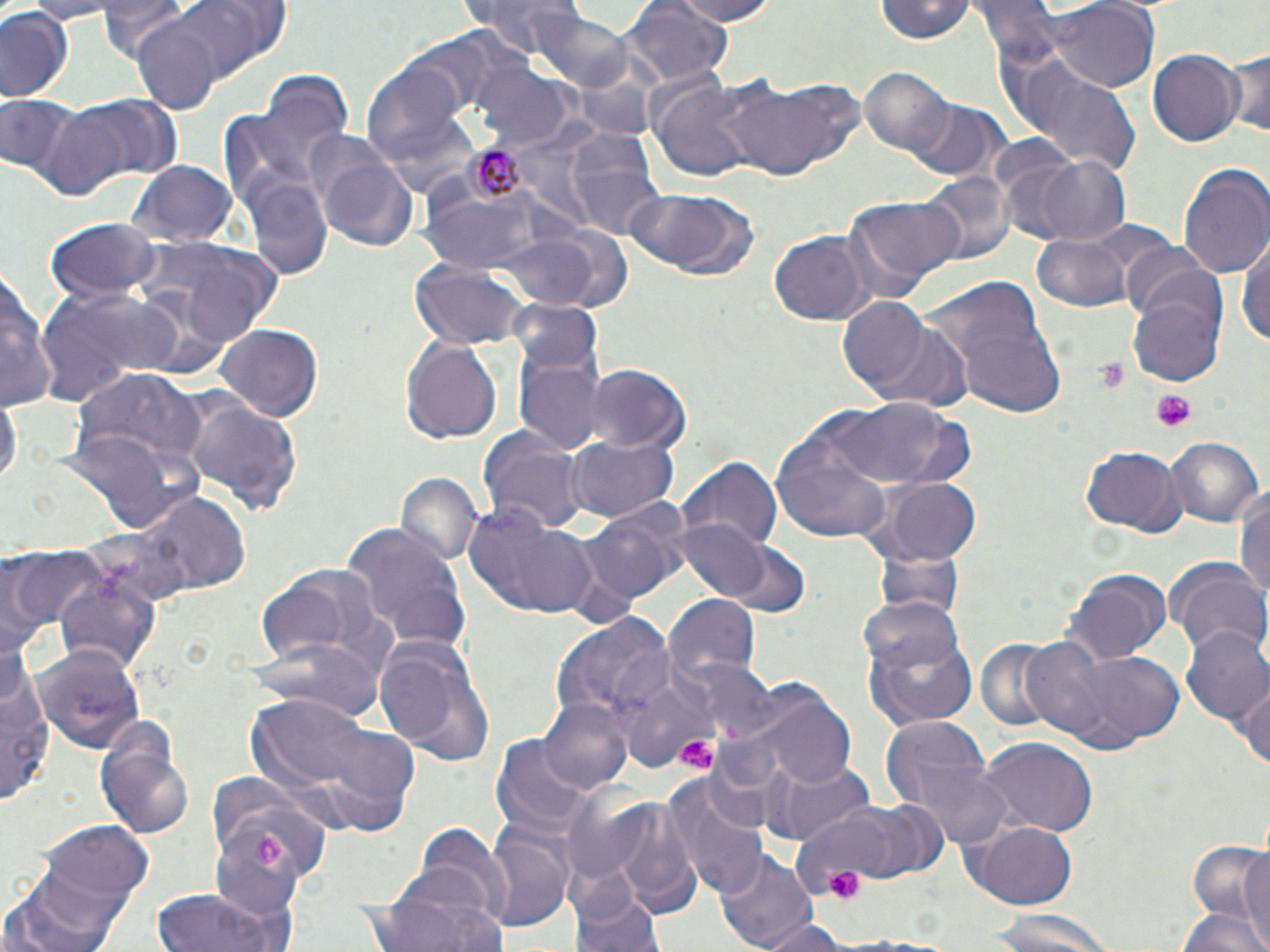 Approximate bounding boxes as named x1/y1/x2/y2 corners in pixels. Plasmodium malariae-infected red blood cell locations: (x1=459, y1=137, x2=545, y2=210). Uninfected red blood cell locations: (x1=93, y1=0, x2=203, y2=71), (x1=159, y1=0, x2=290, y2=78), (x1=453, y1=0, x2=593, y2=49), (x1=662, y1=0, x2=787, y2=25), (x1=872, y1=0, x2=978, y2=45), (x1=625, y1=1, x2=732, y2=87), (x1=0, y1=4, x2=75, y2=106), (x1=1047, y1=4, x2=1159, y2=92), (x1=536, y1=8, x2=634, y2=92), (x1=131, y1=20, x2=219, y2=112), (x1=1224, y1=47, x2=1269, y2=141), (x1=1147, y1=51, x2=1242, y2=146), (x1=1002, y1=54, x2=1141, y2=174), (x1=473, y1=63, x2=569, y2=147), (x1=361, y1=64, x2=459, y2=154), (x1=246, y1=65, x2=354, y2=184), (x1=859, y1=69, x2=956, y2=159), (x1=713, y1=77, x2=856, y2=184), (x1=653, y1=79, x2=761, y2=182), (x1=49, y1=94, x2=181, y2=192), (x1=1, y1=95, x2=79, y2=182), (x1=909, y1=101, x2=1005, y2=182), (x1=564, y1=128, x2=665, y2=236), (x1=306, y1=132, x2=420, y2=253), (x1=1028, y1=155, x2=1133, y2=246), (x1=1178, y1=159, x2=1270, y2=279), (x1=128, y1=162, x2=236, y2=249), (x1=922, y1=170, x2=1010, y2=268), (x1=246, y1=179, x2=334, y2=280), (x1=622, y1=188, x2=761, y2=282), (x1=404, y1=191, x2=540, y2=261), (x1=849, y1=195, x2=967, y2=290), (x1=46, y1=219, x2=161, y2=302), (x1=557, y1=221, x2=641, y2=314), (x1=770, y1=232, x2=871, y2=326), (x1=1033, y1=234, x2=1133, y2=312), (x1=1236, y1=234, x2=1270, y2=352), (x1=130, y1=237, x2=286, y2=351), (x1=1121, y1=241, x2=1215, y2=323), (x1=409, y1=259, x2=529, y2=347), (x1=0, y1=266, x2=53, y2=415), (x1=922, y1=271, x2=1072, y2=423), (x1=1125, y1=273, x2=1230, y2=388), (x1=34, y1=283, x2=189, y2=402), (x1=835, y1=294, x2=946, y2=405), (x1=510, y1=320, x2=609, y2=457), (x1=215, y1=326, x2=323, y2=420), (x1=400, y1=337, x2=503, y2=446), (x1=583, y1=362, x2=691, y2=454), (x1=70, y1=370, x2=208, y2=481), (x1=176, y1=392, x2=305, y2=522), (x1=0, y1=394, x2=20, y2=493), (x1=827, y1=397, x2=970, y2=491), (x1=771, y1=426, x2=895, y2=543), (x1=481, y1=428, x2=585, y2=534), (x1=56, y1=430, x2=183, y2=536), (x1=566, y1=436, x2=678, y2=523), (x1=1166, y1=437, x2=1263, y2=530), (x1=1082, y1=447, x2=1185, y2=535), (x1=678, y1=455, x2=780, y2=553), (x1=395, y1=473, x2=483, y2=571), (x1=866, y1=478, x2=983, y2=561), (x1=1236, y1=484, x2=1270, y2=612), (x1=120, y1=487, x2=250, y2=602), (x1=466, y1=501, x2=597, y2=621), (x1=577, y1=506, x2=683, y2=605), (x1=677, y1=519, x2=770, y2=600), (x1=342, y1=522, x2=472, y2=653), (x1=871, y1=535, x2=963, y2=618), (x1=724, y1=544, x2=811, y2=620), (x1=7, y1=546, x2=110, y2=637), (x1=1168, y1=560, x2=1270, y2=662), (x1=257, y1=565, x2=388, y2=671), (x1=1064, y1=569, x2=1171, y2=666), (x1=55, y1=571, x2=161, y2=676), (x1=663, y1=595, x2=759, y2=687), (x1=552, y1=614, x2=675, y2=734), (x1=862, y1=616, x2=982, y2=730), (x1=1182, y1=626, x2=1270, y2=726), (x1=372, y1=631, x2=495, y2=765), (x1=973, y1=638, x2=1067, y2=732), (x1=35, y1=643, x2=145, y2=754), (x1=1049, y1=643, x2=1189, y2=753), (x1=610, y1=655, x2=720, y2=772), (x1=2, y1=666, x2=54, y2=811), (x1=1232, y1=676, x2=1270, y2=771), (x1=753, y1=689, x2=858, y2=788), (x1=245, y1=693, x2=418, y2=838), (x1=540, y1=697, x2=632, y2=795), (x1=882, y1=716, x2=988, y2=813), (x1=94, y1=725, x2=195, y2=837), (x1=491, y1=734, x2=594, y2=837), (x1=981, y1=737, x2=1096, y2=837), (x1=910, y1=756, x2=1019, y2=849), (x1=765, y1=758, x2=873, y2=844), (x1=664, y1=770, x2=768, y2=895), (x1=598, y1=800, x2=704, y2=916), (x1=844, y1=800, x2=951, y2=883), (x1=962, y1=820, x2=1080, y2=910), (x1=37, y1=822, x2=151, y2=909), (x1=206, y1=823, x2=304, y2=917), (x1=409, y1=823, x2=512, y2=922), (x1=480, y1=829, x2=573, y2=932), (x1=1233, y1=850, x2=1270, y2=946), (x1=713, y1=851, x2=818, y2=952), (x1=1181, y1=863, x2=1268, y2=948), (x1=569, y1=873, x2=665, y2=952), (x1=0, y1=875, x2=129, y2=952), (x1=153, y1=887, x2=296, y2=952), (x1=369, y1=889, x2=505, y2=952), (x1=1177, y1=907, x2=1268, y2=952), (x1=988, y1=911, x2=1118, y2=952), (x1=759, y1=916, x2=854, y2=952). Platelet locations: (x1=1091, y1=358, x2=1131, y2=392), (x1=1150, y1=388, x2=1198, y2=429), (x1=676, y1=735, x2=717, y2=770), (x1=252, y1=833, x2=285, y2=867), (x1=820, y1=857, x2=865, y2=906). Slide-level diagnosis: Plasmodium malariae. Optical microscopy. Image is 1270×952 pixels. Thin blood film. 1000x magnification. One field of a larger specimen. May-Grünwald-Giemsa-stained preparation.